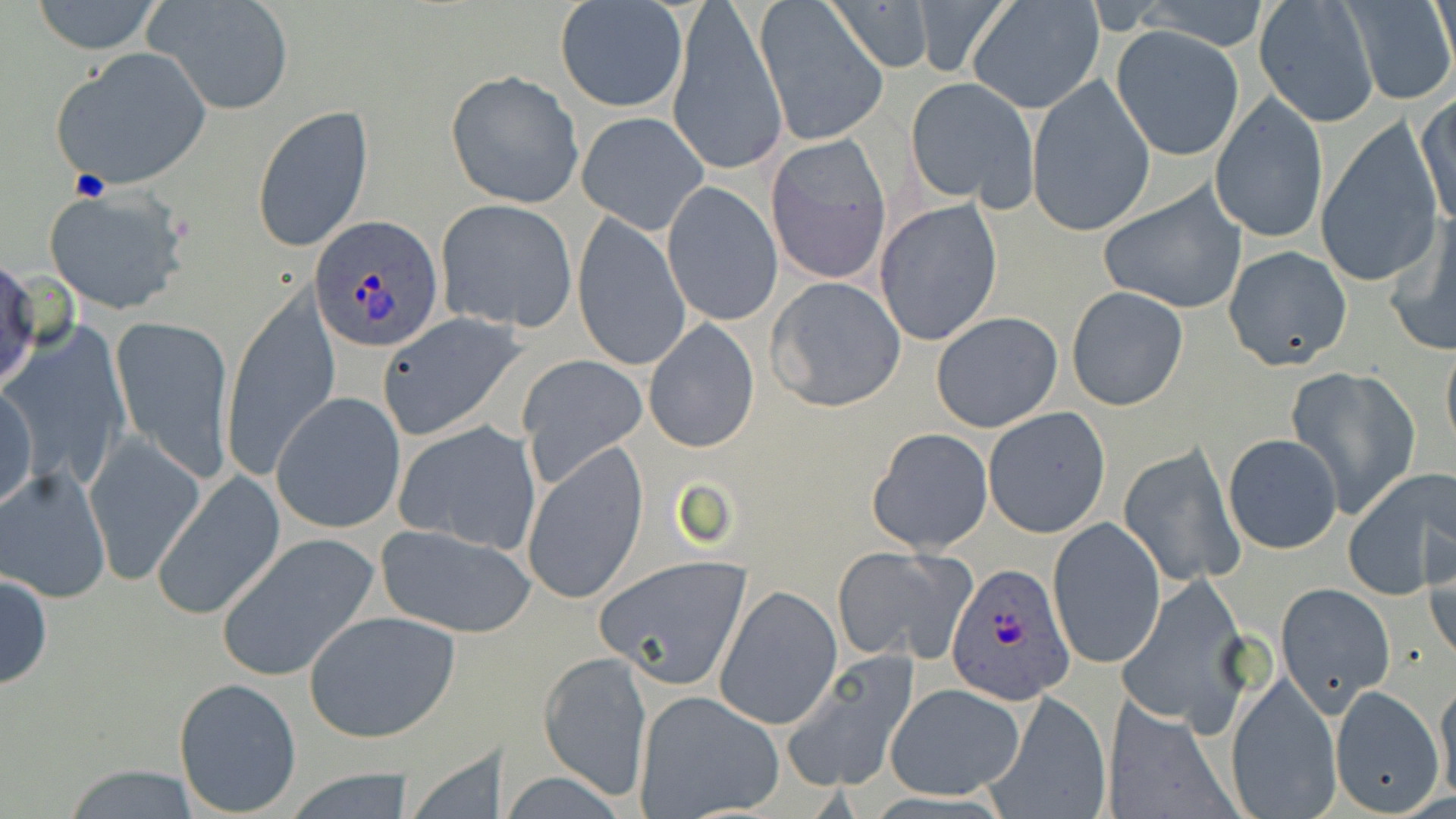
Summary:
  - Coordinate format: approximate bounding boxes as named x1/y1/x2/y2 corners in pixels
  - Uninfected red blood cell locations: (x1=29, y1=0, x2=165, y2=55), (x1=147, y1=0, x2=296, y2=118), (x1=824, y1=0, x2=937, y2=73), (x1=912, y1=0, x2=1015, y2=79), (x1=968, y1=1, x2=1105, y2=114), (x1=1134, y1=1, x2=1272, y2=51), (x1=1253, y1=1, x2=1382, y2=128), (x1=556, y1=2, x2=686, y2=113), (x1=667, y1=2, x2=787, y2=177), (x1=756, y1=2, x2=889, y2=145), (x1=1341, y1=2, x2=1455, y2=105), (x1=1110, y1=25, x2=1245, y2=159), (x1=50, y1=48, x2=212, y2=192), (x1=445, y1=70, x2=584, y2=208), (x1=1027, y1=74, x2=1154, y2=236), (x1=905, y1=76, x2=1040, y2=208), (x1=1415, y1=94, x2=1456, y2=229), (x1=1210, y1=95, x2=1328, y2=242), (x1=253, y1=106, x2=375, y2=255), (x1=578, y1=112, x2=708, y2=234), (x1=1315, y1=120, x2=1444, y2=289), (x1=765, y1=133, x2=891, y2=284), (x1=662, y1=181, x2=782, y2=327), (x1=1099, y1=183, x2=1248, y2=314), (x1=41, y1=186, x2=190, y2=315), (x1=435, y1=199, x2=578, y2=333), (x1=874, y1=199, x2=1004, y2=347), (x1=573, y1=212, x2=691, y2=372), (x1=1384, y1=216, x2=1456, y2=356), (x1=1223, y1=246, x2=1352, y2=371), (x1=0, y1=258, x2=43, y2=394), (x1=765, y1=276, x2=907, y2=412), (x1=1065, y1=285, x2=1190, y2=411), (x1=221, y1=286, x2=338, y2=479), (x1=931, y1=312, x2=1062, y2=431), (x1=377, y1=313, x2=525, y2=441), (x1=113, y1=317, x2=235, y2=487), (x1=644, y1=320, x2=759, y2=453), (x1=4, y1=327, x2=130, y2=494), (x1=1442, y1=341, x2=1456, y2=452), (x1=517, y1=353, x2=647, y2=487), (x1=1284, y1=367, x2=1421, y2=521), (x1=1, y1=385, x2=37, y2=512), (x1=271, y1=393, x2=406, y2=532), (x1=982, y1=406, x2=1112, y2=538), (x1=393, y1=420, x2=542, y2=552), (x1=869, y1=427, x2=993, y2=553), (x1=1222, y1=433, x2=1343, y2=554), (x1=83, y1=434, x2=206, y2=588), (x1=520, y1=442, x2=648, y2=604), (x1=1118, y1=442, x2=1246, y2=589), (x1=0, y1=464, x2=112, y2=601), (x1=1344, y1=470, x2=1452, y2=598), (x1=151, y1=471, x2=286, y2=621), (x1=1048, y1=516, x2=1165, y2=670), (x1=374, y1=526, x2=539, y2=639), (x1=215, y1=531, x2=382, y2=682), (x1=832, y1=546, x2=972, y2=663), (x1=1425, y1=546, x2=1456, y2=666), (x1=597, y1=555, x2=754, y2=687), (x1=0, y1=570, x2=52, y2=690), (x1=1115, y1=574, x2=1258, y2=736), (x1=1275, y1=583, x2=1393, y2=715), (x1=715, y1=584, x2=841, y2=729), (x1=304, y1=611, x2=461, y2=743), (x1=782, y1=649, x2=921, y2=793), (x1=539, y1=650, x2=652, y2=799), (x1=1225, y1=674, x2=1342, y2=818), (x1=174, y1=677, x2=304, y2=815), (x1=884, y1=682, x2=1026, y2=801), (x1=1435, y1=683, x2=1456, y2=807), (x1=1329, y1=686, x2=1445, y2=816), (x1=634, y1=690, x2=785, y2=818), (x1=984, y1=690, x2=1112, y2=816), (x1=1102, y1=698, x2=1241, y2=819), (x1=54, y1=764, x2=211, y2=817)
  - Platelet locations: (x1=68, y1=170, x2=111, y2=202)
  - Plasmodium ovale-infected red blood cell locations: (x1=310, y1=217, x2=443, y2=350), (x1=945, y1=561, x2=1074, y2=706)
  - Slide-level diagnosis: Plasmodium ovale
  - Modality: optical microscopy
  - Stain: May-Grünwald-Giemsa
  - Magnification: 1000x
  - Image size: 1456×819 pixels
  - Preparation: thin blood film
  - Field of view: one of a larger specimen